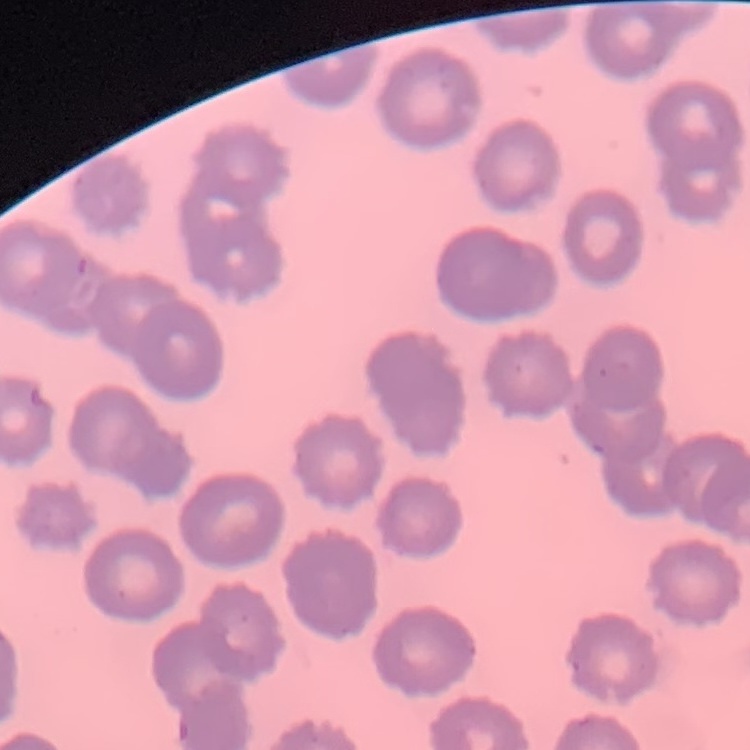

Summary:
  - Erythrocyte morphology: no rouleaux formation
  - Image type: square crop of a larger photomicrograph
  - Stain: Field's or Giemsa
  - Preparation: thin blood film